Locate leukocytes (white blood cells).
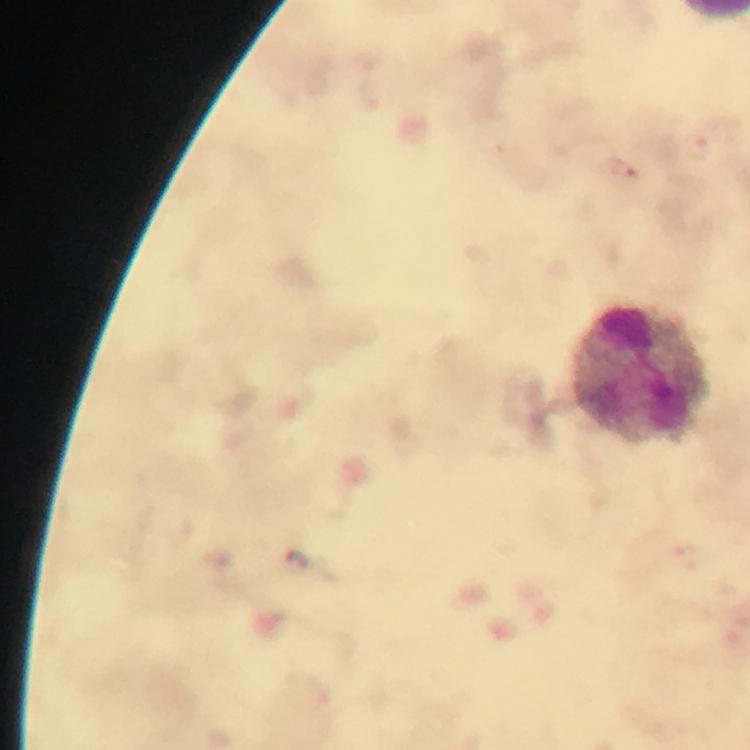

Approximate centers as [x, y] in pixels.
Leukocytes: [642, 375].

immersion oil = applied
stain = Giemsa
magnification = 100x
capture = smartphone mounted on the microscope
cropped from = a single field of view
malaria parasite locations = approximate centers as [x, y] in pixels: [623, 170]
preparation = thick blood smear
image size = 750×750 pixels
context = from a diagnostic examination for malaria